Name the parasite shown.
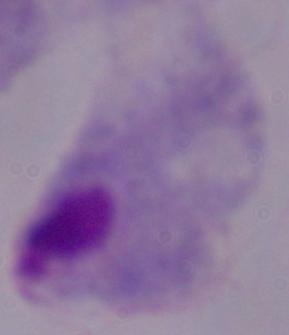

This is a trichomonad.

Summary:
  - Magnification: 1000x
  - Modality: photomicrograph